Classify this cell by malaria status.
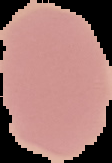

It is uninfected.

Image is 112×163 pixels. From a thin blood smear. Cell region segmented out of the field of view; the surrounding area is masked to black.